Assess this cell for malaria.
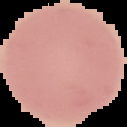

It is uninfected.

image type = segmented cell region on a black background
preparation = thin blood smear
image size = 127×127 pixels